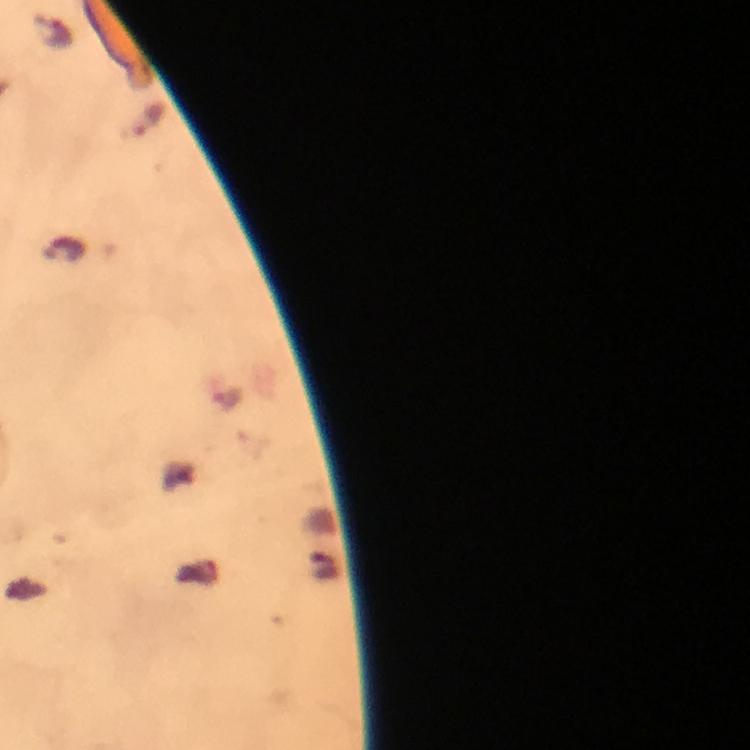

{
  "magnification": "100x",
  "image_size": "750×750 pixels",
  "cropped_from": "a single field of view",
  "stain": "Giemsa",
  "capture": "smartphone mounted on the microscope",
  "preparation": "thick smear",
  "context": "from a diagnostic examination for malaria",
  "immersion_oil": "used",
  "plasmodium_parasite_locations": "approximate centers as [x, y] in pixels: [148, 120]"
}